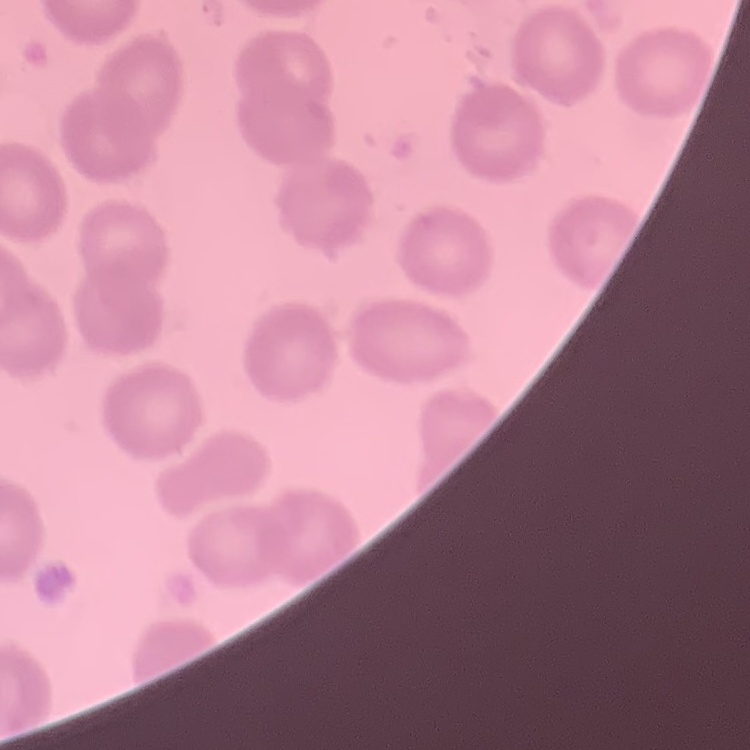
red blood cell morphology = no rouleaux formation
image type = square crop of a larger photomicrograph
stain = Field's or Giemsa
preparation = thin blood film